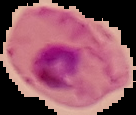

{
  "preparation": "thin blood film",
  "image_size": "136×115 pixels",
  "result": "malaria parasites identified",
  "image_type": "cell region segmented out of the field of view; surrounding area masked to black"
}